State which parasite is depicted.
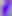

This is Toxoplasma gondii.

{
  "modality": "micrograph",
  "magnification": "400x"
}